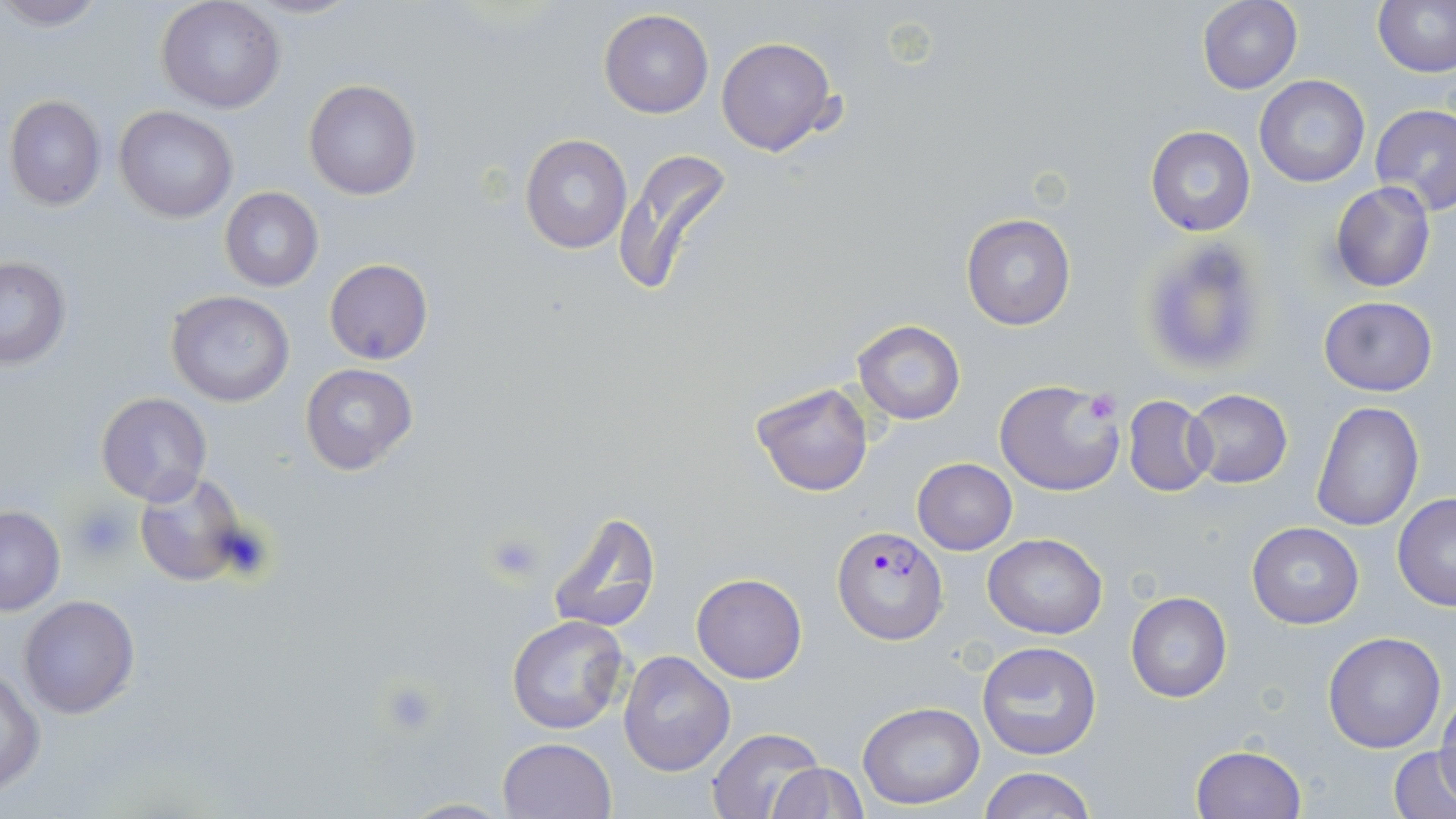
Summary:
  - Coordinate format: approximate bounding boxes as (x1, y1, x2, y2) in pixels
  - Plasmodium falciparum-infected red blood cell locations: (832, 525, 948, 643)
  - Uninfected red blood cell locations: (1, 0, 109, 30), (1372, 0, 1456, 77), (156, 1, 285, 114), (1196, 1, 1303, 94), (599, 8, 713, 118), (716, 35, 840, 156), (1254, 75, 1369, 188), (304, 79, 421, 200), (5, 96, 107, 209), (1370, 103, 1456, 216), (114, 105, 238, 223), (1146, 126, 1255, 237), (520, 135, 633, 255), (613, 147, 733, 298), (1330, 181, 1437, 293), (219, 187, 324, 293), (961, 212, 1075, 331), (1137, 236, 1273, 380), (0, 256, 72, 370), (325, 259, 432, 365), (165, 291, 293, 407), (1319, 295, 1438, 396), (853, 321, 966, 423), (300, 362, 420, 477), (993, 379, 1126, 496), (752, 382, 874, 496), (1186, 389, 1293, 488), (96, 392, 212, 504), (1122, 395, 1217, 496), (1310, 401, 1424, 532), (911, 458, 1018, 555), (134, 471, 254, 589), (1392, 493, 1456, 611), (0, 506, 66, 616), (546, 508, 662, 636), (1246, 522, 1365, 629), (983, 533, 1106, 639), (692, 573, 807, 684), (1125, 592, 1231, 702), (17, 595, 140, 718), (507, 614, 631, 735), (1322, 631, 1447, 753), (976, 640, 1103, 759), (619, 650, 735, 776), (1, 668, 46, 794), (1435, 694, 1456, 804), (857, 701, 985, 808), (705, 729, 825, 817), (497, 737, 617, 819), (1189, 745, 1307, 818), (1390, 747, 1456, 818), (768, 763, 865, 818), (978, 765, 1094, 819), (391, 798, 517, 818)
  - Platelet locations: (1090, 389, 1117, 419), (72, 503, 136, 561), (487, 531, 546, 582)
  - Slide-level diagnosis: Plasmodium falciparum
  - Magnification: 1000x
  - Stain: May-Grünwald-Giemsa
  - Field of view: single
  - Modality: optical microscopy
  - Image size: 1456×819 pixels
  - Preparation: thin blood film